Assess this cell for malaria.
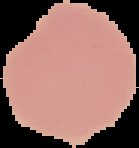

It is uninfected.

Summary:
  - Preparation: thin blood smear
  - Image type: segmented cell region on a black background
  - Image size: 139×148 pixels